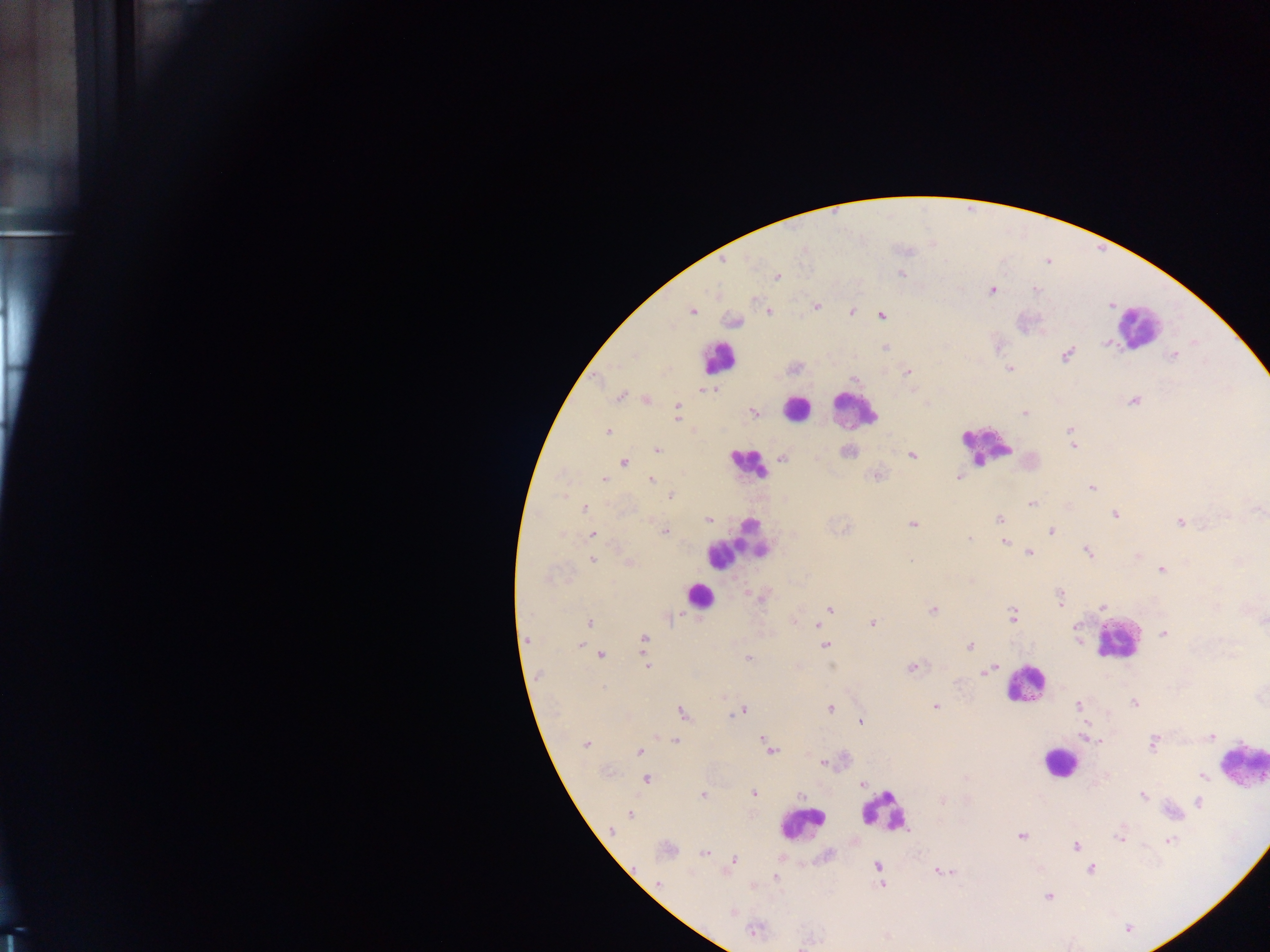

Approximate centers as x y in pixels. Plasmodium parasite locations: 901 273; 777 277; 1036 289; 991 290; 816 306; 692 310; 852 311; 769 312; 881 316; 733 321; 1106 342; 885 347; 1066 354; 1172 356; 1010 368; 906 372; 702 389; 712 389; 620 396; 647 400; 1133 401; 676 407; 753 412; 1025 413; 676 418; 1070 430; 608 431; 1073 446; 657 450; 847 451; 912 455; 782 458; 624 462; 877 475; 959 476; 604 479; 651 479; 1092 487; 671 496; 1031 505; 584 508; 1258 510; 1115 514; 999 519; 709 521; 1180 523; 912 525; 665 531; 1051 532; 561 534; 593 534; 970 539; 1004 542; 1087 551; 1029 552; 1139 556; 592 559; 910 560; 628 562; 1162 570; 548 578; 1060 597; 1102 607; 829 609; 933 610; 1012 616; 672 617; 589 622; 873 623; 818 625; 1163 633; 644 639; 580 645; 824 645; 969 645; 602 655; 748 659; 646 666; 911 668; 986 671; 724 698; 1134 703; 1079 705; 936 707; 831 708; 741 711; 682 712; 860 722; 1211 737; 1087 738; 675 741; 765 741; 586 744; 1153 744; 770 748; 639 752; 822 763; 1202 777; 647 779; 862 784; 754 793; 802 795; 1142 795; 703 796; 942 801; 1199 802; 629 813; 611 830; 1021 835; 1120 838; 1169 841; 1076 846; 666 850; 704 853; 734 860; 877 865; 1091 869; 943 872; 775 877; 658 882; 881 885; 1048 896; 732 913; 753 931. Leukocyte locations: 1145 326; 719 358; 796 408; 854 409; 986 446; 747 464; 735 547; 697 595; 1115 639; 1023 685; 1058 762; 1247 767; 885 811; 801 824. Thick blood film. One field of view. Collected in Ghana. Mobile-phone photograph taken through the microscope. Image is 1270×952 pixels.